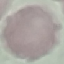
Summary:
  - Malaria status: uninfected
  - Capture: smartphone through the microscope eyepiece
  - Preparation: thin smear
  - Stain: Giemsa
  - Image type: automatically extracted cell patch, resized to 64 × 64 pixels